Outline Plasmodium malariae parasites and classify them by life-cycle stage.
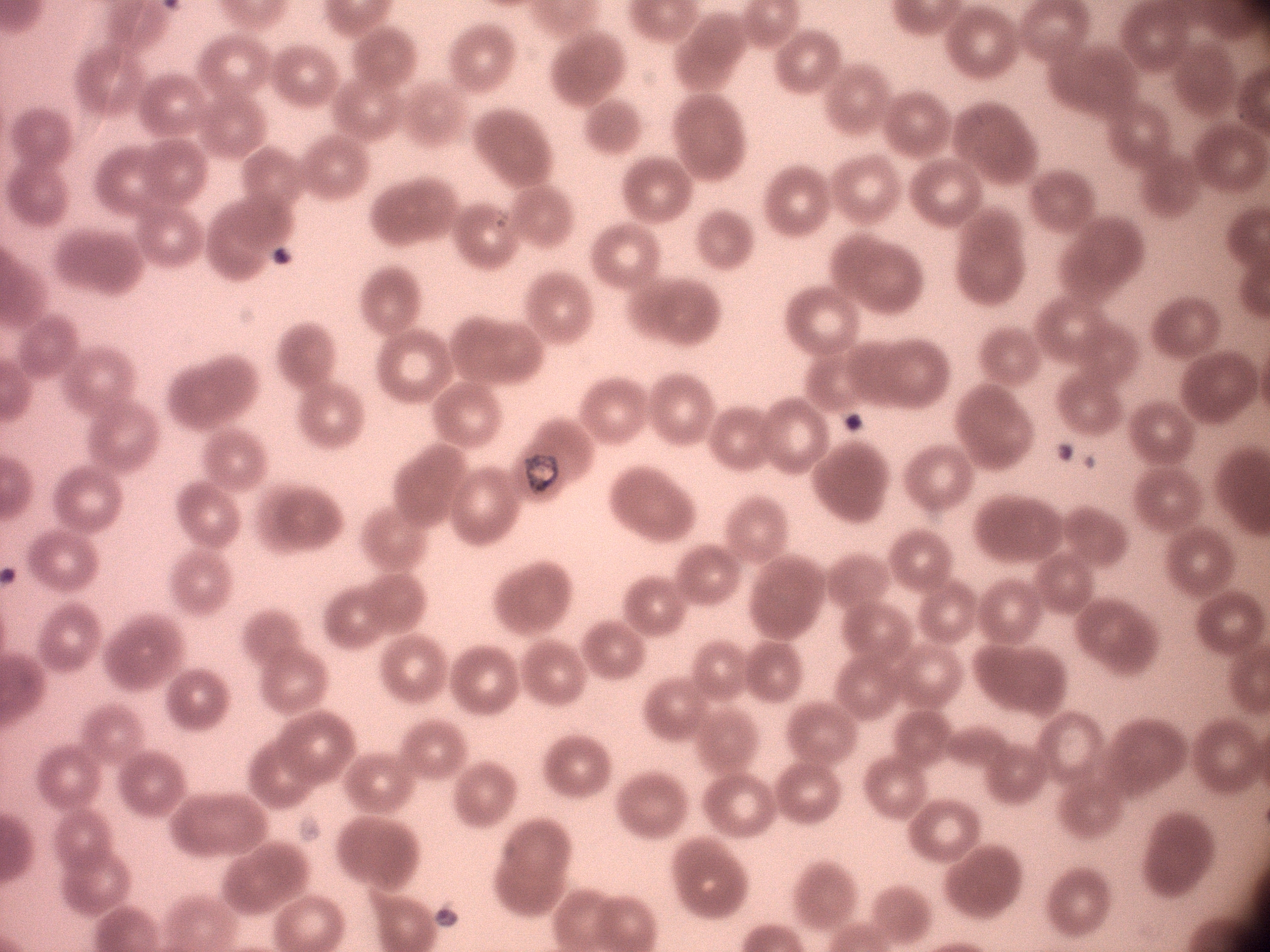

Approximate bounding boxes as [x1, y1, x2, y2] in pixels, from the source annotation, which is not necessarily exhaustive.
Trophozoites: [525, 451, 559, 494].

species = Plasmodium malariae
field of view = single
magnification = 100x
stain = Giemsa
microscope = Leica DM2000 with built-in camera
preparation = thin blood film
image size = 1270×952 pixels